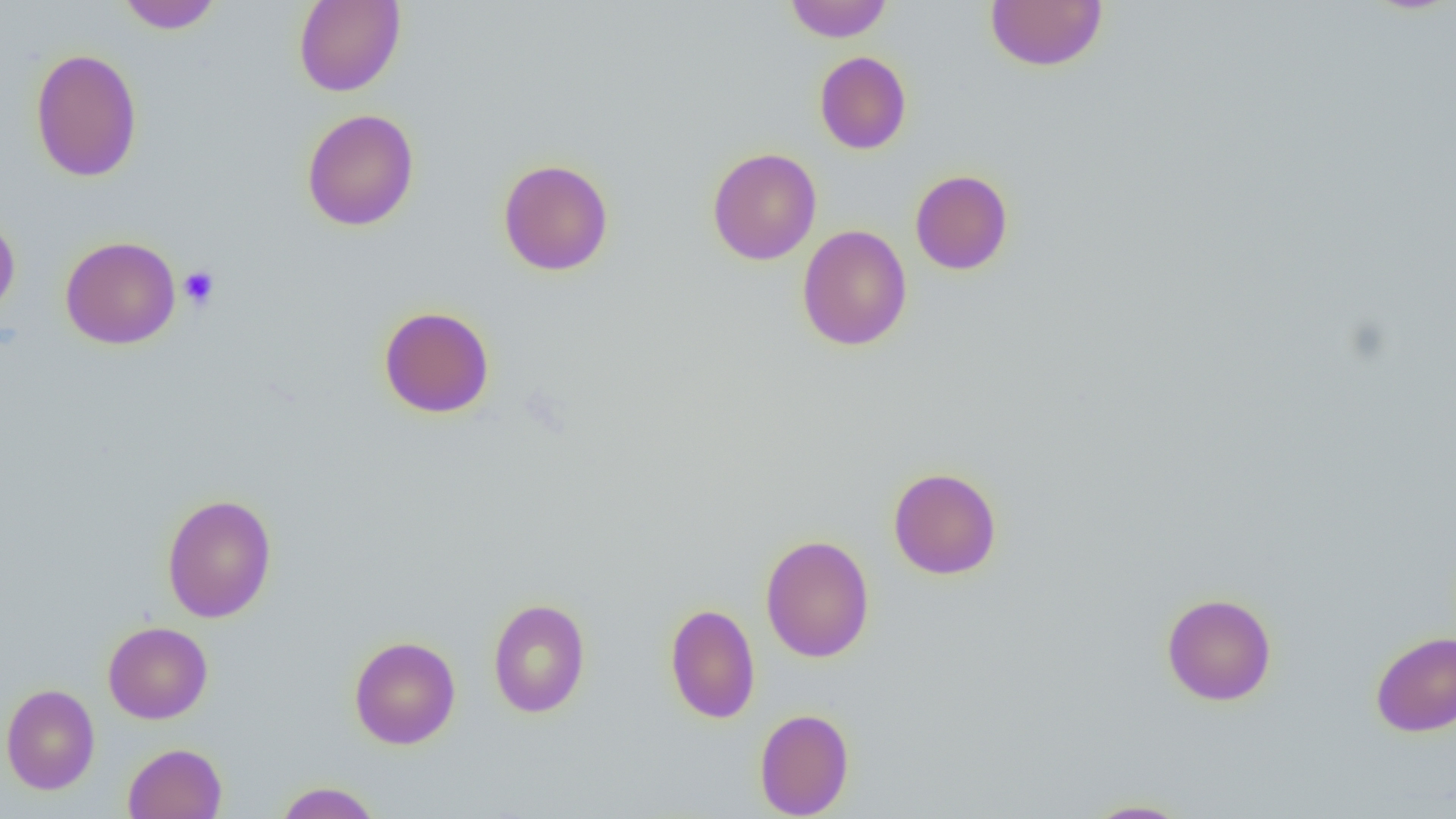

Approximate bounding boxes as (x1,y1)-(x2,y2) corner pairs in pixels. Platelet locations: (179,266)-(220,310). Uninfected red blood cell locations: (117,0)-(223,33), (293,0)-(406,97), (985,0)-(1108,72), (784,1)-(892,42), (30,48)-(143,182), (814,51)-(912,154), (302,109)-(420,231), (707,147)-(821,265), (498,158)-(614,276), (910,169)-(1013,275), (0,215)-(20,318), (796,225)-(912,351), (60,236)-(181,350), (378,306)-(495,418), (887,466)-(1002,580), (161,494)-(277,623), (760,534)-(875,663), (1161,592)-(1277,706), (488,598)-(591,718), (665,602)-(761,723), (103,621)-(213,724), (1370,630)-(1456,737), (349,635)-(461,749), (1,683)-(100,794), (754,708)-(855,818), (123,743)-(227,819), (274,781)-(383,818), (1081,799)-(1195,818). Slide-level diagnosis: no evidence of blood parasites. Captured at 1000x magnification. Image is 1456×819 pixels. Thin blood smear. Single field of view. Light microscopy.